Describe the morphology of the erythrocytes.
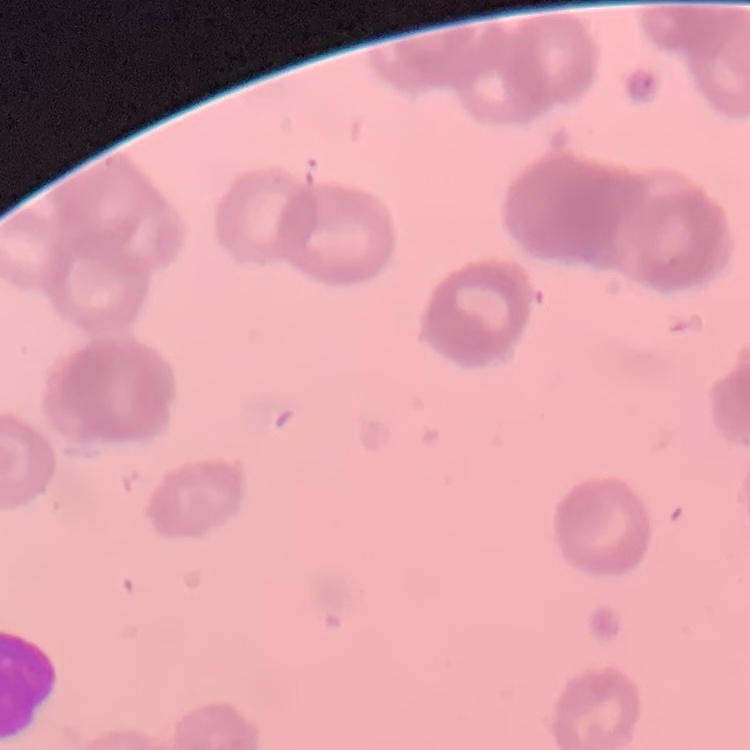
They show rouleaux formation.

stain: Field's or Giemsa
preparation: thin blood film
image_type: one tile cut from a larger photomicrograph